Draw a bounding box around every leukocyte (white blood cell).
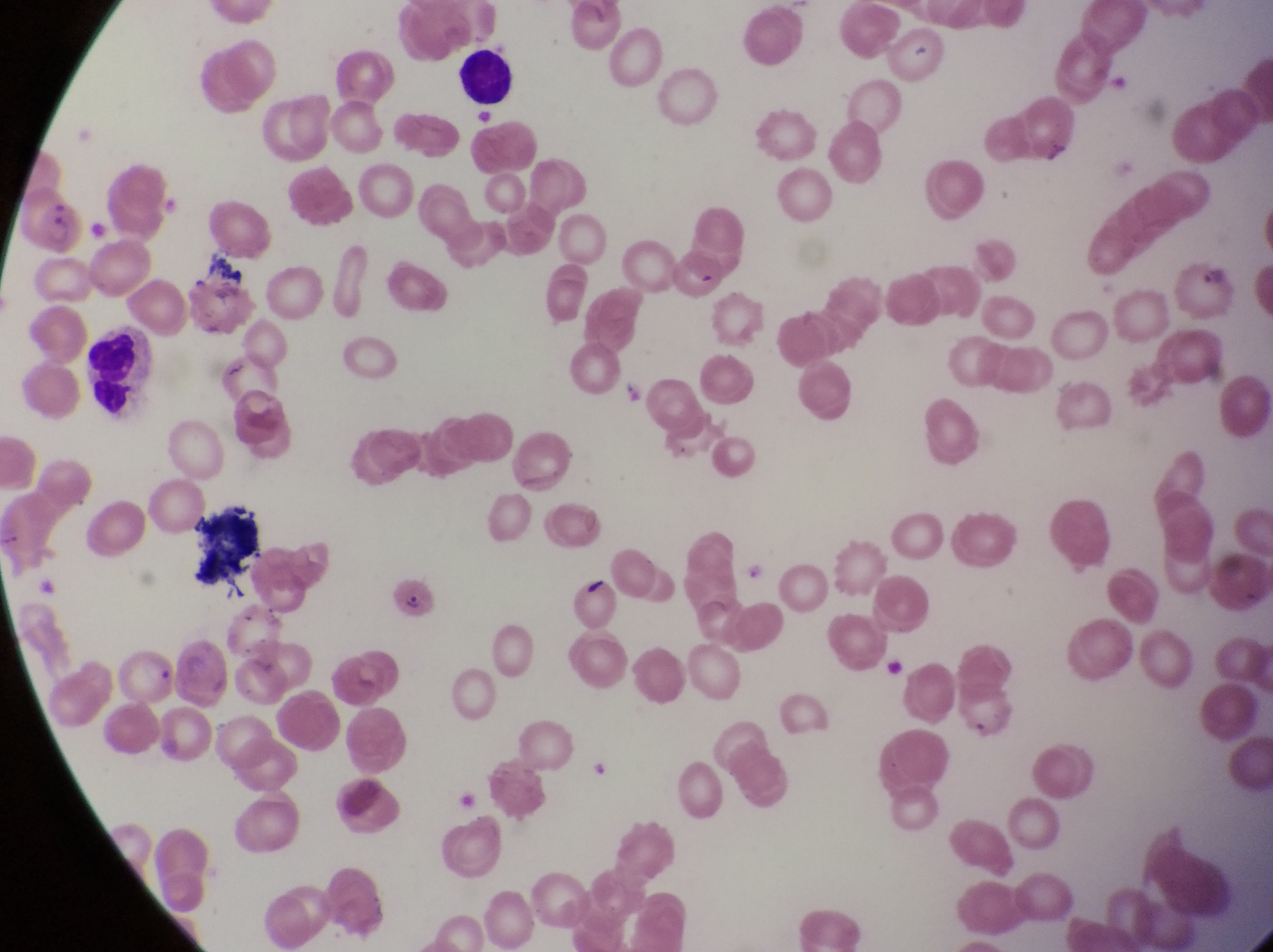

Approximate bounding boxes as {left, top, right, bottom} in pixels.
Leukocytes: {454, 45, 521, 119}, {81, 325, 152, 411}.
One object is labeled both leukocyte and artifact (platelet-like body, stain precipitate, or debris) by the source: {187, 505, 265, 590}.

Parasitised red blood cell locations: {28, 193, 88, 256}, {667, 252, 730, 305}, {1180, 252, 1240, 326}, {387, 577, 439, 624}. Artifact (platelet-like body, stain precipitate, or debris) locations: {1039, 140, 1081, 173}, {577, 572, 614, 604}. Image is 1273×952 pixels. One field of view. Photographed through the eyepiece of an Olympus CX-23 microscope with a smartphone camera. At a magnification of 1000x. Thin blood smear. Collected in Uganda.